Classify this cell by malaria status.
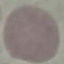

Uninfected.

Thin blood film. Automatically extracted cell patch, resized to 64 × 64 pixels. Photographed with a smartphone camera at the microscope eyepiece. Giemsa-stained preparation.